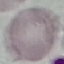
Result: negative for malaria parasites. Giemsa stain. Acquired by smartphone through the microscope eyepiece. Thin blood film. Automatically extracted cell patch, resized to 64 × 64 pixels.